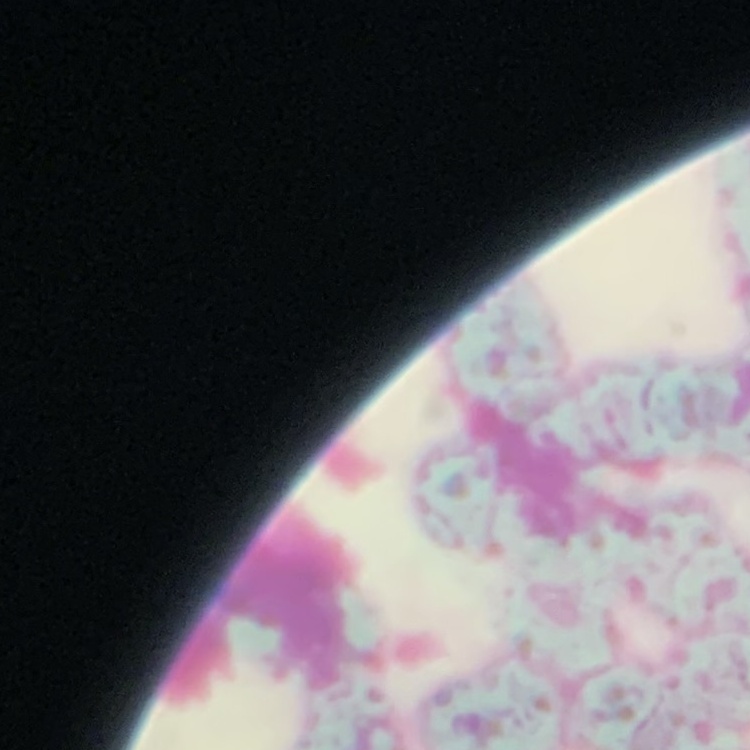

The erythrocytes exhibit rouleaux formation. Thin peripheral smear. Square crop of a larger photomicrograph. Field's or Giemsa stain.